Comment on the morphology of the red blood cells.
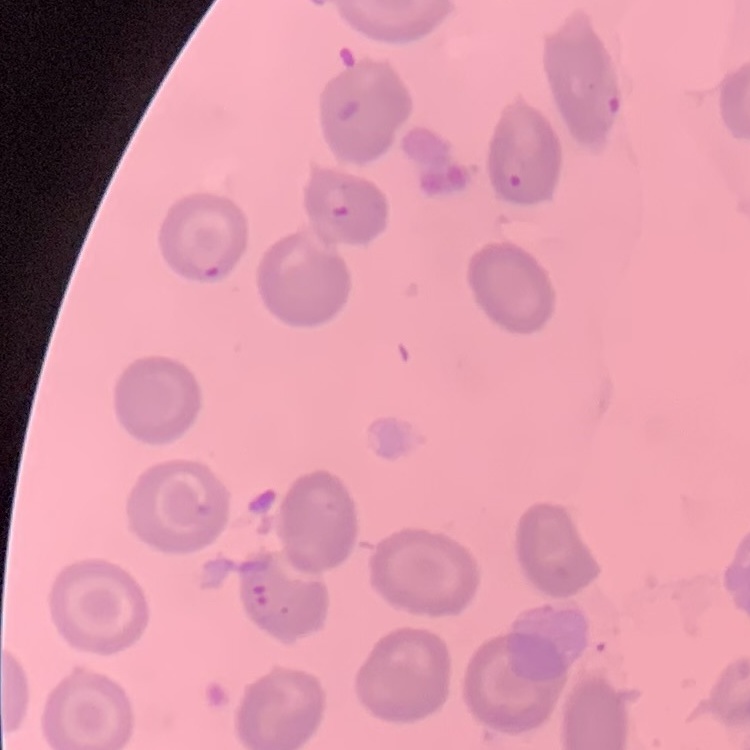

They show no rouleaux formation.

{
  "preparation": "thin peripheral smear",
  "image_type": "one tile cut from a larger photomicrograph",
  "stain": "Field's or Giemsa"
}